Name the parasite shown.
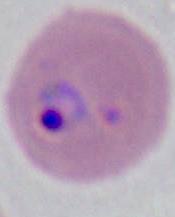
This is Plasmodium.

Summary:
  - Magnification: 400x or 1000x
  - Modality: micrograph